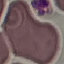

Summary:
  - Result: negative for malaria parasites
  - Image type: automatically extracted cell patch, resized to 64 × 64 pixels
  - Preparation: thin blood film
  - Capture: smartphone through the microscope eyepiece
  - Stain: Giemsa